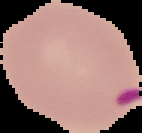
The area outside the segmented cell region is set to black. Image is 142×133 pixels. Malaria status: parasitized. From a thin blood smear.